Classify this cell by malaria status.
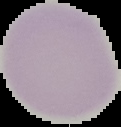
Uninfected.

Segmented cell region on a black background. From a thin blood film. Image is 121×127 pixels.